Name the parasite shown.
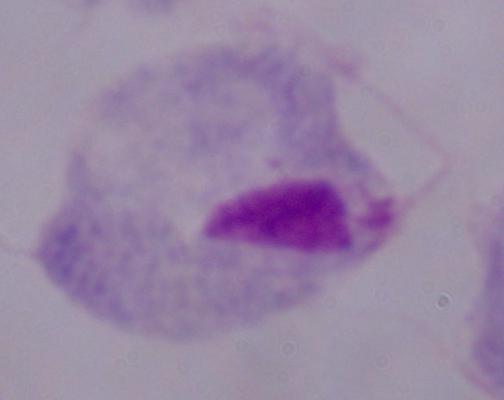
A trichomonad.

Summary:
  - Modality: micrograph
  - Magnification: 1000x